Classify this cell by malaria status.
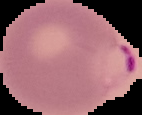

It is parasitized.

Summary:
  - Preparation: thin blood smear
  - Image size: 142×115 pixels
  - Image type: segmented cell region with the area outside set to black